Report the malaria status of this cell.
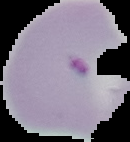

Parasitized.

image size = 130×142 pixels
image type = segmented cell region with the area outside set to black
preparation = thin blood film